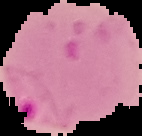 Result: malaria parasites detected. Image is 142×136 pixels. Cell region segmented out of the field of view; the surrounding area is masked to black. From a thin blood smear.